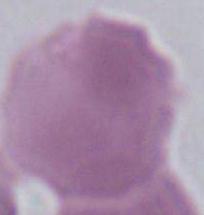

A red blood cell is shown. Captured at 1000x magnification. Photomicrograph.